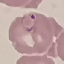
malaria status = parasitized
preparation = thin blood film
capture = smartphone through the microscope eyepiece
image type = automatically extracted cell patch, resized to 64 × 64 pixels
stain = Giemsa